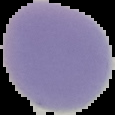
Summary:
  - Malaria status: uninfected
  - Image type: cell region segmented out of the field of view; surrounding area masked to black
  - Preparation: thin blood smear
  - Image size: 115×115 pixels